Identify the parasite.
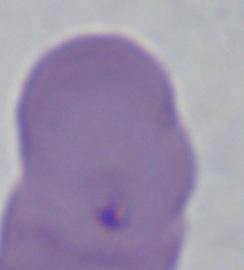

This is Babesia.

{
  "modality": "photomicrograph",
  "magnification": "1000x"
}